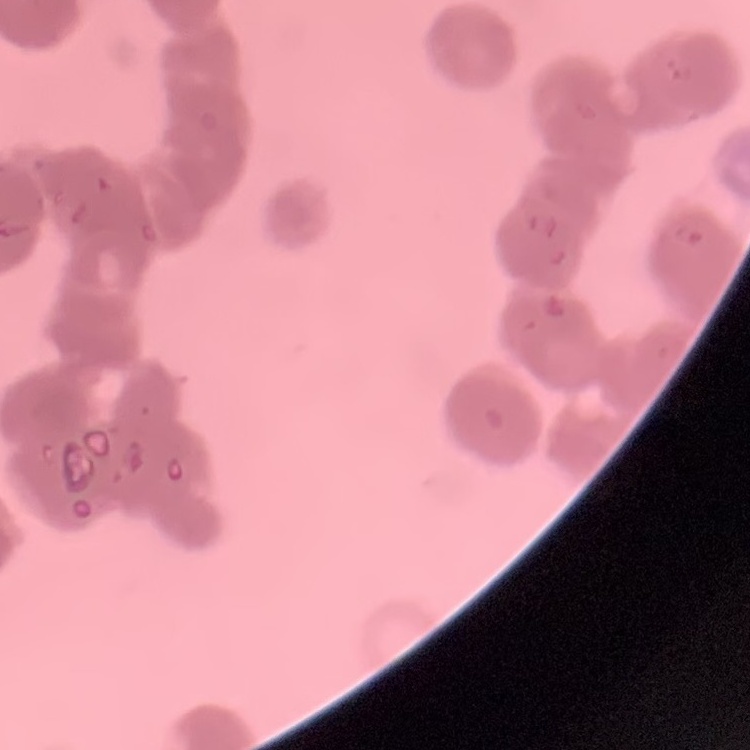
Summary:
  - Red blood cell morphology: rouleaux formation
  - Image type: one tile cut from a larger photomicrograph
  - Stain: Field's or Giemsa
  - Preparation: thin blood smear